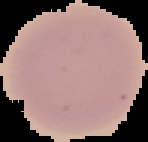 Malaria status: uninfected. Image is 148×142 pixels. Cell region segmented out of the field of view; the surrounding area is masked to black. From a thin blood smear.